Report the malaria status of this cell.
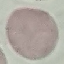
Uninfected.

capture = smartphone through the microscope eyepiece
preparation = thin blood film
stain = Giemsa
image type = cell patch, automatically extracted from a larger field of view and resized to 64 × 64 pixels